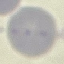

malaria status = uninfected
stain = Giemsa
capture = smartphone through the microscope eyepiece
image type = cell patch, automatically extracted from a larger field of view and resized to 64 × 64 pixels
preparation = thin smear